Outline each blood parasite and name the species.
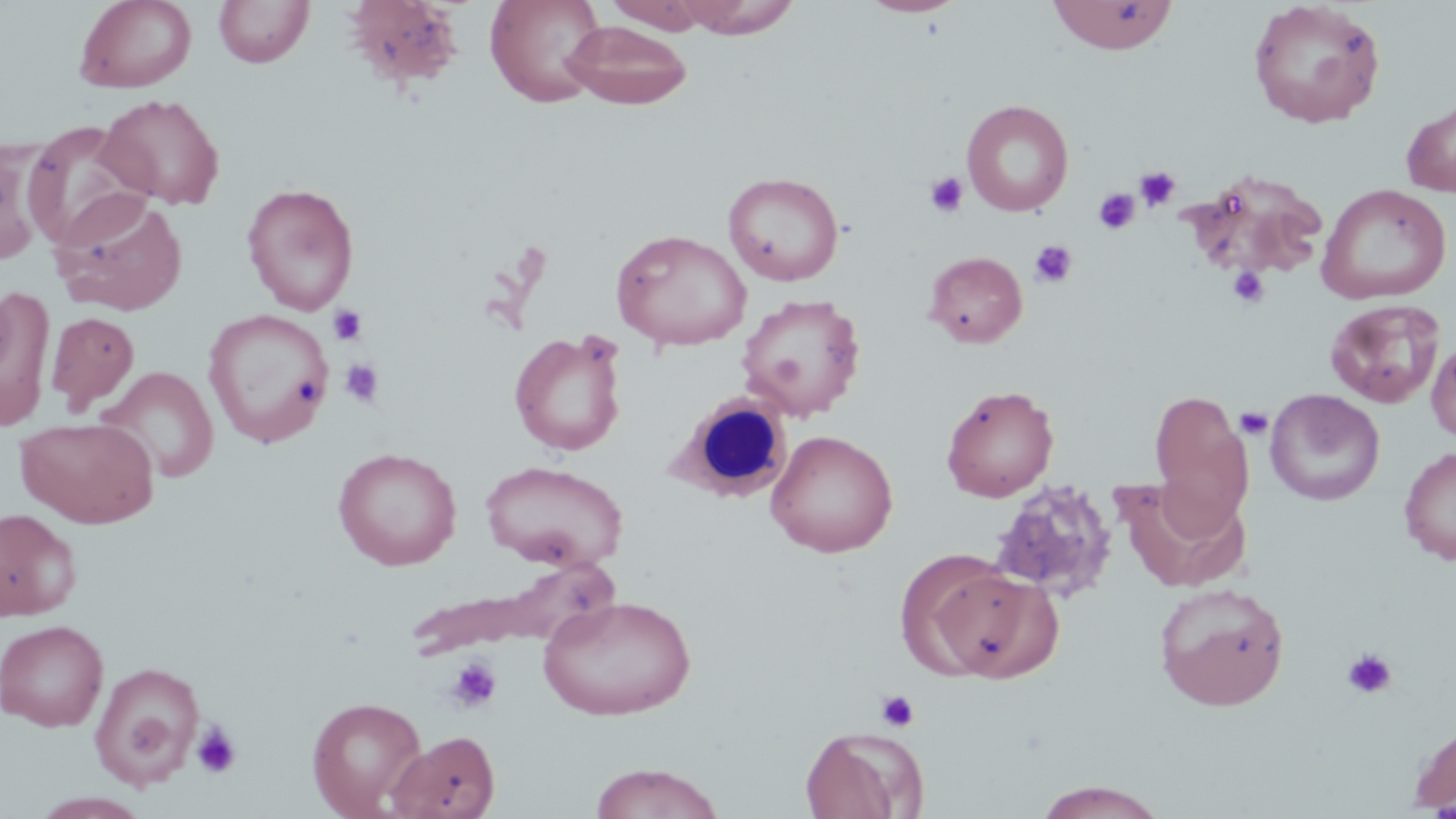

No blood parasites observed.

Approximate bounding boxes as named x1/y1/x2/y2 corners in pixels. Uninfected red blood cell locations (subset): (x1=73, y1=0, x2=197, y2=93), (x1=485, y1=0, x2=607, y2=108), (x1=605, y1=0, x2=711, y2=34), (x1=676, y1=0, x2=800, y2=39), (x1=859, y1=0, x2=967, y2=18), (x1=1047, y1=0, x2=1178, y2=54), (x1=1247, y1=0, x2=1387, y2=129), (x1=213, y1=1, x2=314, y2=68), (x1=343, y1=1, x2=466, y2=92), (x1=562, y1=20, x2=692, y2=109), (x1=98, y1=93, x2=226, y2=210), (x1=961, y1=99, x2=1074, y2=216), (x1=1401, y1=99, x2=1456, y2=197), (x1=22, y1=121, x2=152, y2=250), (x1=0, y1=136, x2=60, y2=261), (x1=1184, y1=170, x2=1331, y2=283), (x1=723, y1=172, x2=844, y2=286), (x1=1316, y1=182, x2=1452, y2=305), (x1=241, y1=183, x2=360, y2=315), (x1=50, y1=192, x2=189, y2=316), (x1=610, y1=229, x2=752, y2=351), (x1=924, y1=251, x2=1027, y2=348), (x1=0, y1=283, x2=55, y2=429), (x1=735, y1=293, x2=866, y2=421), (x1=1324, y1=298, x2=1446, y2=409), (x1=203, y1=308, x2=335, y2=448), (x1=45, y1=311, x2=139, y2=413), (x1=508, y1=330, x2=627, y2=457), (x1=1427, y1=336, x2=1456, y2=444), (x1=96, y1=366, x2=219, y2=483), (x1=940, y1=385, x2=1059, y2=503), (x1=1148, y1=388, x2=1253, y2=531), (x1=1265, y1=389, x2=1385, y2=506), (x1=16, y1=417, x2=158, y2=528), (x1=766, y1=430, x2=898, y2=558), (x1=1399, y1=446, x2=1456, y2=564), (x1=332, y1=447, x2=462, y2=570), (x1=481, y1=460, x2=628, y2=572), (x1=987, y1=478, x2=1118, y2=605), (x1=1117, y1=479, x2=1251, y2=592), (x1=0, y1=508, x2=81, y2=621), (x1=927, y1=565, x2=1061, y2=682), (x1=1154, y1=583, x2=1289, y2=711), (x1=537, y1=594, x2=696, y2=721), (x1=0, y1=619, x2=109, y2=731), (x1=90, y1=661, x2=205, y2=787), (x1=307, y1=696, x2=428, y2=817), (x1=1409, y1=720, x2=1456, y2=815), (x1=799, y1=726, x2=926, y2=818), (x1=388, y1=730, x2=500, y2=819), (x1=589, y1=762, x2=725, y2=819), (x1=1033, y1=781, x2=1170, y2=818), (x1=29, y1=792, x2=152, y2=819). Platelet locations: (x1=1134, y1=166, x2=1180, y2=211), (x1=925, y1=172, x2=968, y2=218), (x1=1093, y1=187, x2=1139, y2=234), (x1=1029, y1=239, x2=1078, y2=288), (x1=1228, y1=265, x2=1271, y2=309), (x1=327, y1=304, x2=367, y2=346), (x1=340, y1=358, x2=385, y2=407), (x1=1234, y1=407, x2=1273, y2=439), (x1=1343, y1=649, x2=1398, y2=699), (x1=446, y1=656, x2=502, y2=713), (x1=875, y1=690, x2=919, y2=733), (x1=191, y1=721, x2=242, y2=778). Slide-level diagnosis: no evidence of blood parasites. Image is 1456×819 pixels. Thin blood film. May-Grünwald-Giemsa stain. 1000x magnification. Light microscopy. One field of a larger specimen.